Outline each blood parasite and name the species.
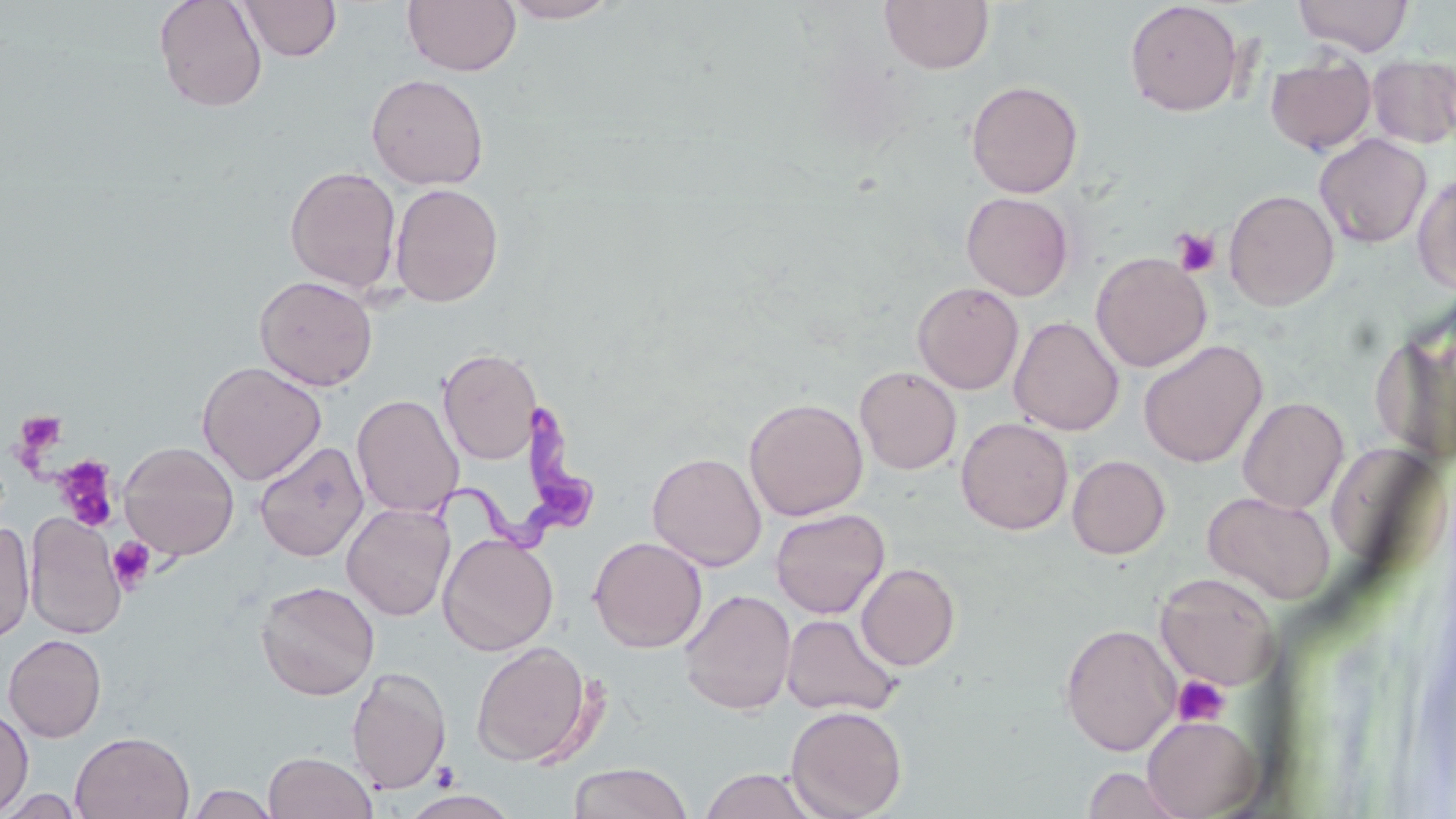
Approximate bounding boxes as (x1,y1)-(x2,y2) corner pairs in pixels.
Trypanosoma brucei: (429,388)-(598,558).
No Plasmodium falciparum, Plasmodium ovale, Plasmodium malariae, Plasmodium vivax, or Babesia divergens observed.

Summary:
  - Uninfected red blood cell locations: (153,0)-(268,112), (402,0)-(520,77), (500,0)-(623,23), (879,0)-(993,74), (1292,0)-(1414,56), (238,1)-(342,62), (1124,1)-(1244,117), (1366,53)-(1455,150), (1265,55)-(1376,154), (366,73)-(489,190), (965,80)-(1083,198), (1314,133)-(1432,248), (284,165)-(402,295), (1413,172)-(1456,296), (389,183)-(503,307), (1224,188)-(1340,311), (961,191)-(1074,301), (1091,252)-(1212,372), (254,274)-(378,391), (912,282)-(1024,394), (1371,304)-(1456,468), (1008,316)-(1124,436), (1138,340)-(1268,468), (439,348)-(542,465), (197,361)-(327,486), (854,365)-(962,475), (352,394)-(464,518), (1237,396)-(1349,513), (743,397)-(869,521), (956,417)-(1073,535), (254,440)-(369,561), (118,441)-(240,560), (1325,441)-(1446,574), (647,451)-(767,571), (1067,455)-(1170,559), (1202,490)-(1336,604), (342,502)-(455,621), (770,508)-(890,619), (25,513)-(126,639), (0,520)-(36,642), (437,533)-(559,656), (588,536)-(708,653), (856,563)-(960,671), (1156,573)-(1280,691), (255,580)-(380,700), (679,589)-(796,715), (781,612)-(904,718), (1059,622)-(1182,756), (3,634)-(107,742), (470,641)-(595,767), (347,666)-(451,794), (786,704)-(908,819), (0,706)-(33,815), (1141,714)-(1263,818), (70,731)-(194,819), (263,750)-(378,819), (568,762)-(692,819), (1080,765)-(1193,819), (698,768)-(819,818), (184,785)-(282,819), (0,789)-(84,818), (401,790)-(521,818)
  - Platelet locations: (1172,228)-(1221,278), (15,410)-(68,459), (53,455)-(120,532), (107,537)-(157,592), (1173,676)-(1229,726)
  - Slide-level diagnosis: Trypanosoma brucei
  - Magnification: 1000x
  - Stain: May-Grünwald-Giemsa
  - Preparation: thin blood film
  - Image size: 1456×819 pixels
  - Field of view: one of a larger specimen
  - Modality: light microscopy